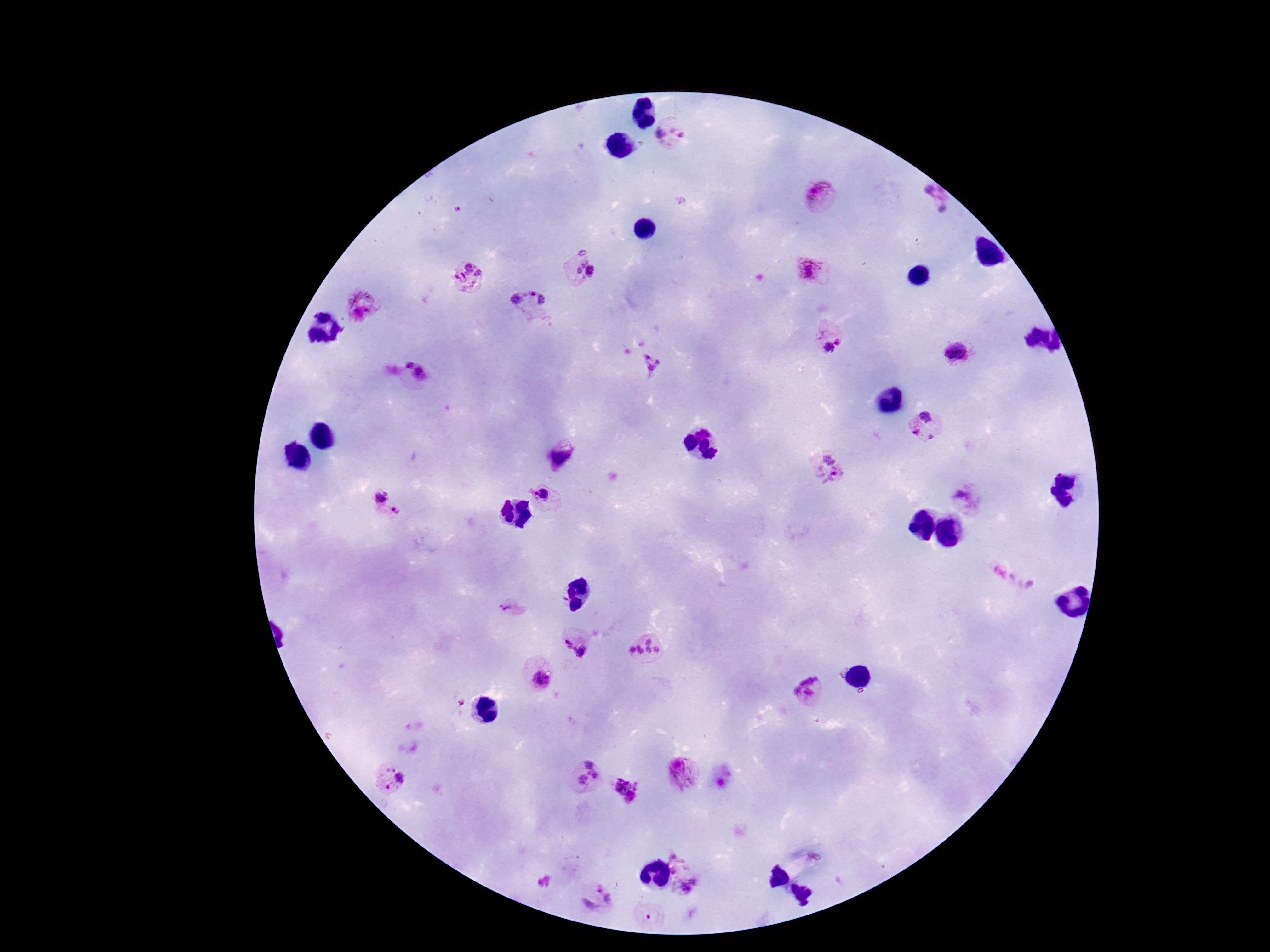 Approximate centers as [x, y] in pixels. Plasmodium parasite locations: [672, 138], [822, 193], [934, 202], [809, 269], [578, 270], [469, 276], [364, 306], [530, 307], [829, 334], [956, 353], [649, 366], [417, 372], [925, 426], [561, 460], [830, 469], [540, 494], [379, 495], [970, 496], [398, 511], [1010, 579], [510, 608], [567, 642], [646, 650], [584, 654], [542, 680], [810, 692], [581, 774], [683, 774], [391, 780], [625, 790], [681, 863], [689, 887], [598, 899], [650, 916]. 100x magnification. Giemsa stain. Patient malaria status: infected. Smartphone photograph taken through the microscope eyepiece. Thick peripheral-blood smear. One field from this slide. Image is 1270×952 pixels.